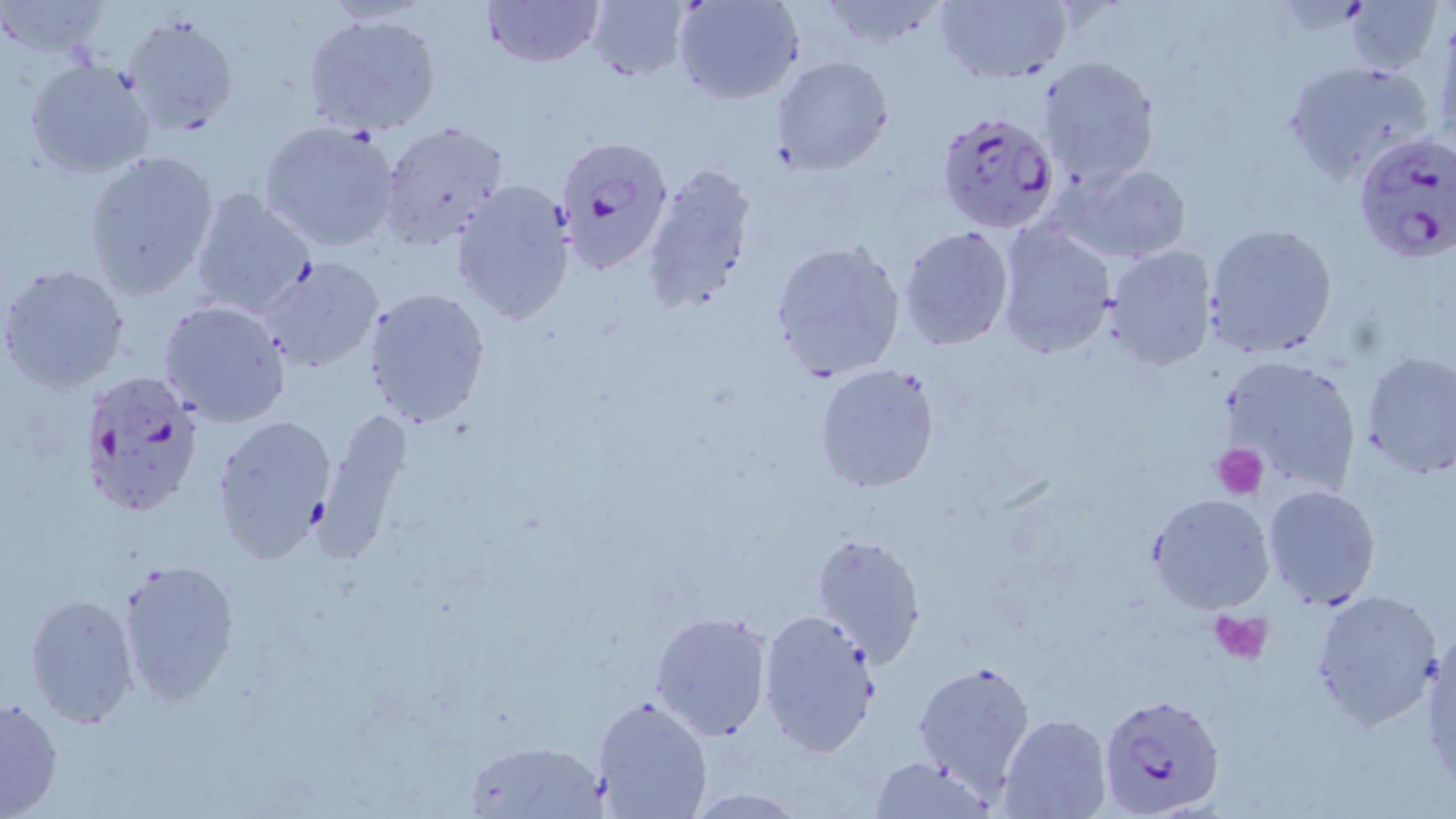

Summary:
  - Coordinate format: approximate bounding boxes as named x1/y1/x2/y2 corners in pixels
  - Platelet locations: (x1=1213, y1=443, x2=1268, y2=498), (x1=1209, y1=607, x2=1274, y2=665)
  - Uninfected red blood cell locations: (x1=479, y1=0, x2=604, y2=68), (x1=584, y1=0, x2=690, y2=81), (x1=673, y1=0, x2=805, y2=105), (x1=814, y1=0, x2=951, y2=54), (x1=0, y1=1, x2=112, y2=60), (x1=934, y1=1, x2=1071, y2=85), (x1=1344, y1=1, x2=1443, y2=77), (x1=304, y1=11, x2=444, y2=136), (x1=120, y1=12, x2=243, y2=138), (x1=1037, y1=55, x2=1161, y2=190), (x1=769, y1=56, x2=893, y2=175), (x1=23, y1=58, x2=157, y2=180), (x1=1281, y1=59, x2=1440, y2=184), (x1=258, y1=119, x2=401, y2=254), (x1=379, y1=121, x2=510, y2=248), (x1=82, y1=149, x2=220, y2=300), (x1=1050, y1=159, x2=1194, y2=265), (x1=640, y1=162, x2=758, y2=316), (x1=451, y1=179, x2=579, y2=328), (x1=188, y1=186, x2=318, y2=319), (x1=993, y1=221, x2=1117, y2=359), (x1=1203, y1=223, x2=1338, y2=360), (x1=897, y1=225, x2=1015, y2=350), (x1=768, y1=238, x2=907, y2=383), (x1=1102, y1=245, x2=1217, y2=371), (x1=255, y1=255, x2=384, y2=373), (x1=1, y1=263, x2=131, y2=393), (x1=361, y1=286, x2=490, y2=429), (x1=158, y1=299, x2=293, y2=427), (x1=1358, y1=349, x2=1456, y2=480), (x1=1216, y1=354, x2=1365, y2=497), (x1=812, y1=362, x2=941, y2=494), (x1=316, y1=406, x2=414, y2=554), (x1=213, y1=411, x2=338, y2=563), (x1=1262, y1=484, x2=1381, y2=608), (x1=1146, y1=493, x2=1276, y2=613), (x1=810, y1=532, x2=927, y2=666), (x1=112, y1=558, x2=242, y2=705), (x1=1310, y1=589, x2=1440, y2=730), (x1=24, y1=591, x2=140, y2=728), (x1=757, y1=609, x2=883, y2=759), (x1=649, y1=611, x2=775, y2=742), (x1=1421, y1=629, x2=1454, y2=786), (x1=913, y1=659, x2=1035, y2=795), (x1=590, y1=695, x2=714, y2=819), (x1=1, y1=696, x2=65, y2=819), (x1=999, y1=713, x2=1110, y2=819), (x1=462, y1=736, x2=611, y2=817), (x1=867, y1=755, x2=996, y2=819)
  - Plasmodium falciparum-infected red blood cell locations: (x1=934, y1=109, x2=1061, y2=232), (x1=1355, y1=132, x2=1456, y2=265), (x1=550, y1=133, x2=673, y2=272), (x1=76, y1=366, x2=208, y2=519), (x1=1096, y1=692, x2=1226, y2=819)
  - Slide-level diagnosis: Plasmodium falciparum
  - Preparation: thin blood film
  - Field of view: one of a larger specimen
  - Magnification: 1000x
  - Stain: May-Grünwald-Giemsa
  - Image size: 1456×819 pixels
  - Modality: light microscopy